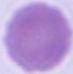
magnification = 1000x
identification = red blood cell
modality = micrograph